Identify the blood parasite species.
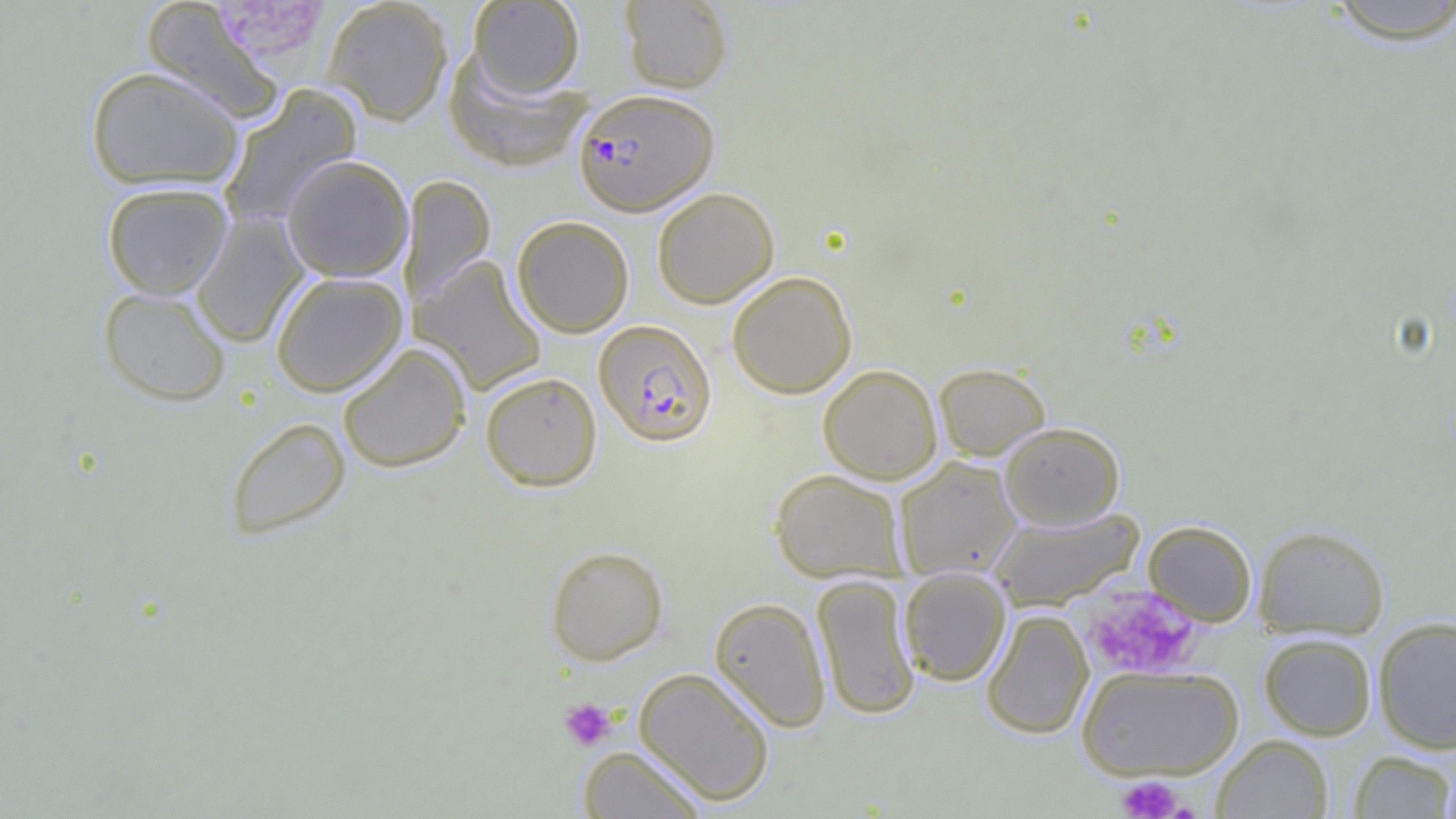
Plasmodium falciparum.

preparation = thin blood film
Plasmodium falciparum-infected red blood cell locations = approximate bounding boxes as (x1,y1)-(x2,y2) corner pairs in pixels: (574,88)-(719,215), (594,319)-(718,447)
field of view = single
uninfected red blood cell locations = approximate bounding boxes as (x1,y1)-(x2,y2) corner pairs in pixels: (322,0)-(454,125), (1319,0)-(1456,45), (142,1)-(285,124), (468,1)-(585,98), (619,1)-(734,93), (443,51)-(592,172), (85,66)-(245,191), (219,84)-(363,228), (281,154)-(414,283), (400,175)-(496,306), (101,181)-(233,299), (652,187)-(780,307), (191,211)-(310,348), (512,215)-(634,337), (412,256)-(547,395), (270,271)-(407,397), (726,271)-(857,398), (97,286)-(232,407), (337,342)-(471,472), (933,362)-(1051,461), (818,364)-(943,484), (481,371)-(602,491), (224,417)-(351,540), (999,421)-(1125,529), (894,456)-(1022,580), (769,469)-(907,583), (988,506)-(1144,611), (1143,520)-(1257,626), (1252,524)-(1390,640), (544,545)-(669,665), (898,568)-(1011,686), (811,574)-(921,720), (709,596)-(832,732), (981,608)-(1094,739), (1372,616)-(1456,754), (1259,633)-(1376,740), (1076,664)-(1245,782), (633,666)-(776,806), (1212,735)-(1334,818), (577,745)-(708,818), (1348,750)-(1455,818), (1436,761)-(1456,819)
platelet locations = approximate bounding boxes as (x1,y1)-(x2,y2) corner pairs in pixels: (216,0)-(324,62), (1084,586)-(1201,680), (559,697)-(617,751), (1116,776)-(1186,818)
image size = 1456×819 pixels
modality = optical microscopy
magnification = 1000x